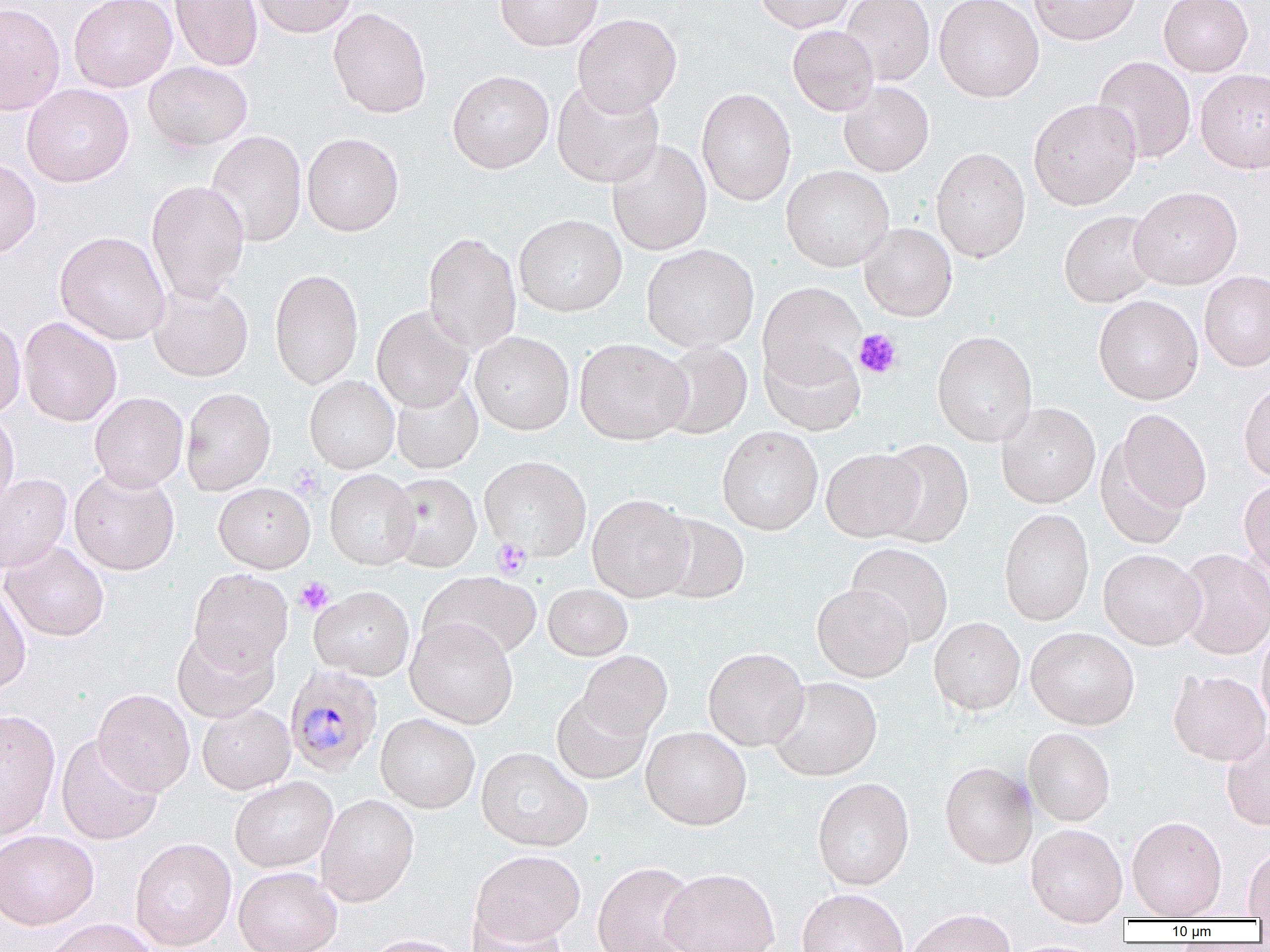 Approximate bounding boxes as named x1/y1/x2/y2 corners in pixels. Platelet locations: (x1=853, y1=329, x2=902, y2=379), (x1=288, y1=464, x2=324, y2=500), (x1=491, y1=538, x2=532, y2=579), (x1=295, y1=577, x2=334, y2=615). Uninfected red blood cell locations: (x1=69, y1=0, x2=177, y2=92), (x1=169, y1=0, x2=263, y2=71), (x1=249, y1=0, x2=358, y2=38), (x1=494, y1=0, x2=603, y2=51), (x1=753, y1=0, x2=856, y2=33), (x1=840, y1=0, x2=934, y2=85), (x1=934, y1=0, x2=1044, y2=102), (x1=1029, y1=0, x2=1140, y2=46), (x1=1158, y1=0, x2=1253, y2=77), (x1=0, y1=2, x2=66, y2=115), (x1=328, y1=7, x2=432, y2=118), (x1=572, y1=13, x2=682, y2=116), (x1=787, y1=25, x2=879, y2=116), (x1=1092, y1=56, x2=1196, y2=164), (x1=143, y1=61, x2=253, y2=151), (x1=1195, y1=68, x2=1270, y2=174), (x1=447, y1=70, x2=554, y2=173), (x1=551, y1=79, x2=664, y2=188), (x1=838, y1=81, x2=934, y2=176), (x1=21, y1=84, x2=134, y2=188), (x1=696, y1=88, x2=796, y2=205), (x1=1028, y1=98, x2=1141, y2=211), (x1=205, y1=131, x2=307, y2=247), (x1=302, y1=133, x2=404, y2=236), (x1=606, y1=140, x2=712, y2=256), (x1=931, y1=147, x2=1031, y2=262), (x1=0, y1=155, x2=42, y2=261), (x1=781, y1=165, x2=894, y2=271), (x1=146, y1=180, x2=250, y2=304), (x1=1129, y1=186, x2=1243, y2=289), (x1=1058, y1=210, x2=1160, y2=308), (x1=514, y1=214, x2=626, y2=317), (x1=859, y1=223, x2=957, y2=322), (x1=54, y1=231, x2=171, y2=345), (x1=422, y1=231, x2=522, y2=355), (x1=641, y1=244, x2=759, y2=353), (x1=269, y1=268, x2=364, y2=389), (x1=1199, y1=271, x2=1270, y2=372), (x1=148, y1=280, x2=253, y2=382), (x1=758, y1=281, x2=865, y2=388), (x1=1093, y1=294, x2=1204, y2=404), (x1=371, y1=306, x2=474, y2=412), (x1=0, y1=316, x2=26, y2=419), (x1=19, y1=317, x2=122, y2=427), (x1=932, y1=330, x2=1038, y2=446), (x1=470, y1=331, x2=575, y2=435), (x1=574, y1=337, x2=691, y2=445), (x1=656, y1=341, x2=753, y2=439), (x1=759, y1=341, x2=866, y2=437), (x1=304, y1=375, x2=399, y2=474), (x1=390, y1=377, x2=483, y2=474), (x1=1238, y1=381, x2=1270, y2=483), (x1=180, y1=387, x2=276, y2=496), (x1=89, y1=392, x2=189, y2=492), (x1=996, y1=402, x2=1100, y2=508), (x1=1114, y1=409, x2=1212, y2=515), (x1=0, y1=411, x2=20, y2=516), (x1=717, y1=425, x2=823, y2=535), (x1=876, y1=439, x2=974, y2=549), (x1=1095, y1=441, x2=1194, y2=551), (x1=821, y1=448, x2=926, y2=542), (x1=479, y1=457, x2=591, y2=560), (x1=69, y1=467, x2=180, y2=576), (x1=324, y1=469, x2=420, y2=570), (x1=0, y1=473, x2=72, y2=574), (x1=386, y1=473, x2=482, y2=573), (x1=1239, y1=478, x2=1270, y2=573), (x1=213, y1=482, x2=315, y2=573), (x1=587, y1=494, x2=694, y2=603), (x1=998, y1=507, x2=1094, y2=626), (x1=653, y1=513, x2=750, y2=605), (x1=1238, y1=538, x2=1269, y2=627), (x1=1, y1=541, x2=109, y2=642), (x1=847, y1=543, x2=953, y2=646), (x1=1175, y1=547, x2=1270, y2=660), (x1=1098, y1=549, x2=1205, y2=650), (x1=188, y1=568, x2=293, y2=673), (x1=419, y1=572, x2=542, y2=662), (x1=0, y1=583, x2=31, y2=695), (x1=812, y1=583, x2=915, y2=682), (x1=543, y1=584, x2=633, y2=661), (x1=309, y1=586, x2=414, y2=681), (x1=928, y1=617, x2=1025, y2=715), (x1=406, y1=618, x2=518, y2=729), (x1=1256, y1=626, x2=1270, y2=727), (x1=171, y1=627, x2=280, y2=723), (x1=1025, y1=627, x2=1139, y2=730), (x1=703, y1=647, x2=810, y2=751), (x1=577, y1=651, x2=672, y2=740), (x1=1168, y1=670, x2=1270, y2=766), (x1=768, y1=677, x2=883, y2=781), (x1=93, y1=688, x2=195, y2=796), (x1=551, y1=690, x2=652, y2=785), (x1=197, y1=704, x2=295, y2=794), (x1=0, y1=709, x2=61, y2=840), (x1=376, y1=714, x2=480, y2=813), (x1=640, y1=727, x2=752, y2=830), (x1=1023, y1=728, x2=1116, y2=826), (x1=1221, y1=728, x2=1270, y2=831), (x1=56, y1=734, x2=164, y2=846), (x1=476, y1=747, x2=592, y2=851), (x1=940, y1=761, x2=1037, y2=868), (x1=230, y1=776, x2=338, y2=873), (x1=812, y1=777, x2=915, y2=890), (x1=316, y1=793, x2=419, y2=907), (x1=1127, y1=816, x2=1227, y2=919), (x1=1025, y1=824, x2=1127, y2=927), (x1=0, y1=830, x2=99, y2=930), (x1=130, y1=837, x2=237, y2=950), (x1=1243, y1=844, x2=1270, y2=919), (x1=471, y1=850, x2=585, y2=948), (x1=592, y1=861, x2=700, y2=952), (x1=234, y1=866, x2=343, y2=952), (x1=660, y1=867, x2=780, y2=952), (x1=797, y1=888, x2=909, y2=952), (x1=905, y1=908, x2=1016, y2=952), (x1=468, y1=912, x2=569, y2=952), (x1=40, y1=918, x2=159, y2=952), (x1=362, y1=933, x2=470, y2=952). Plasmodium malariae-infected red blood cell locations: (x1=284, y1=664, x2=383, y2=776). Slide-level diagnosis: Plasmodium malariae. One field of a larger specimen. Image is 1270×952 pixels. Captured at 1000x magnification. Optical microscopy. Thin blood smear.